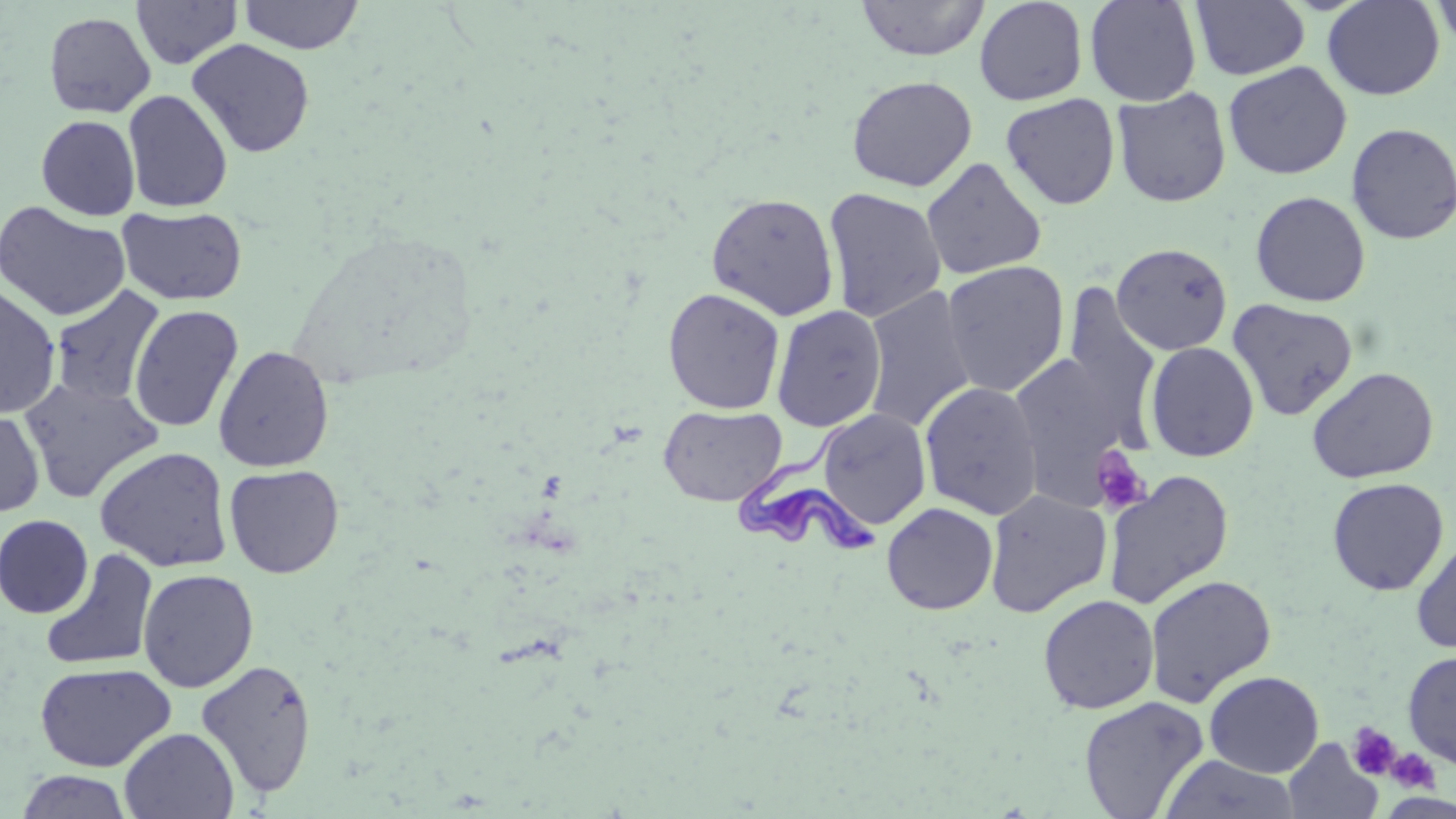
{
  "slide_level_diagnosis": "Trypanosoma brucei",
  "image_size": "1456×819 pixels",
  "stain": "May-Grünwald-Giemsa",
  "trypanosoma_brucei_locations": "approximate bounding boxes as (x1, y1, x2, y2) in pixels: (732, 408, 880, 559)",
  "magnification": "1000x",
  "modality": "optical microscopy",
  "uninfected_red_blood_cell_locations": "approximate bounding boxes as (x1, y1, x2, y2) in pixels: (131, 0, 243, 69), (238, 0, 364, 55), (856, 0, 989, 61), (974, 0, 1088, 106), (1085, 0, 1202, 106), (1322, 0, 1445, 100), (1430, 0, 1456, 51), (1191, 1, 1310, 80), (43, 11, 156, 118), (187, 38, 315, 158), (1223, 61, 1352, 179), (847, 75, 977, 192), (1112, 87, 1231, 208), (122, 89, 233, 212), (1000, 93, 1120, 210), (36, 115, 140, 220), (1346, 122, 1456, 246), (922, 157, 1047, 280), (823, 187, 947, 324), (1250, 191, 1370, 307), (706, 192, 839, 321), (0, 200, 130, 322), (117, 206, 248, 305), (1112, 243, 1232, 355), (941, 260, 1070, 397), (0, 283, 61, 419), (50, 285, 165, 407), (862, 286, 977, 433), (1062, 286, 1162, 439), (663, 288, 785, 414), (1227, 298, 1358, 421), (128, 304, 244, 433), (771, 305, 887, 432), (1145, 342, 1259, 462), (213, 345, 334, 472), (1010, 350, 1141, 504), (1307, 367, 1439, 484), (18, 377, 166, 503), (920, 381, 1043, 520), (658, 405, 787, 507), (0, 407, 44, 517), (817, 408, 931, 531), (94, 446, 233, 572), (224, 464, 345, 578), (1103, 470, 1234, 610), (1327, 477, 1449, 595), (985, 489, 1111, 618), (882, 502, 998, 615), (0, 514, 94, 618), (1411, 537, 1456, 653), (41, 549, 158, 672), (137, 568, 259, 692), (1144, 574, 1277, 707), (1038, 594, 1159, 714), (1402, 650, 1456, 769), (195, 659, 318, 798), (34, 662, 176, 772), (1204, 671, 1324, 777), (1079, 695, 1209, 818), (119, 727, 239, 818), (1283, 738, 1382, 819), (1159, 754, 1301, 818), (15, 770, 134, 818)",
  "field_of_view": "one of a larger specimen",
  "preparation": "thin blood smear",
  "platelet_locations": "approximate bounding boxes as (x1, y1, x2, y2) in pixels: (1089, 445, 1152, 516), (1346, 722, 1400, 779), (1385, 749, 1438, 793)"
}